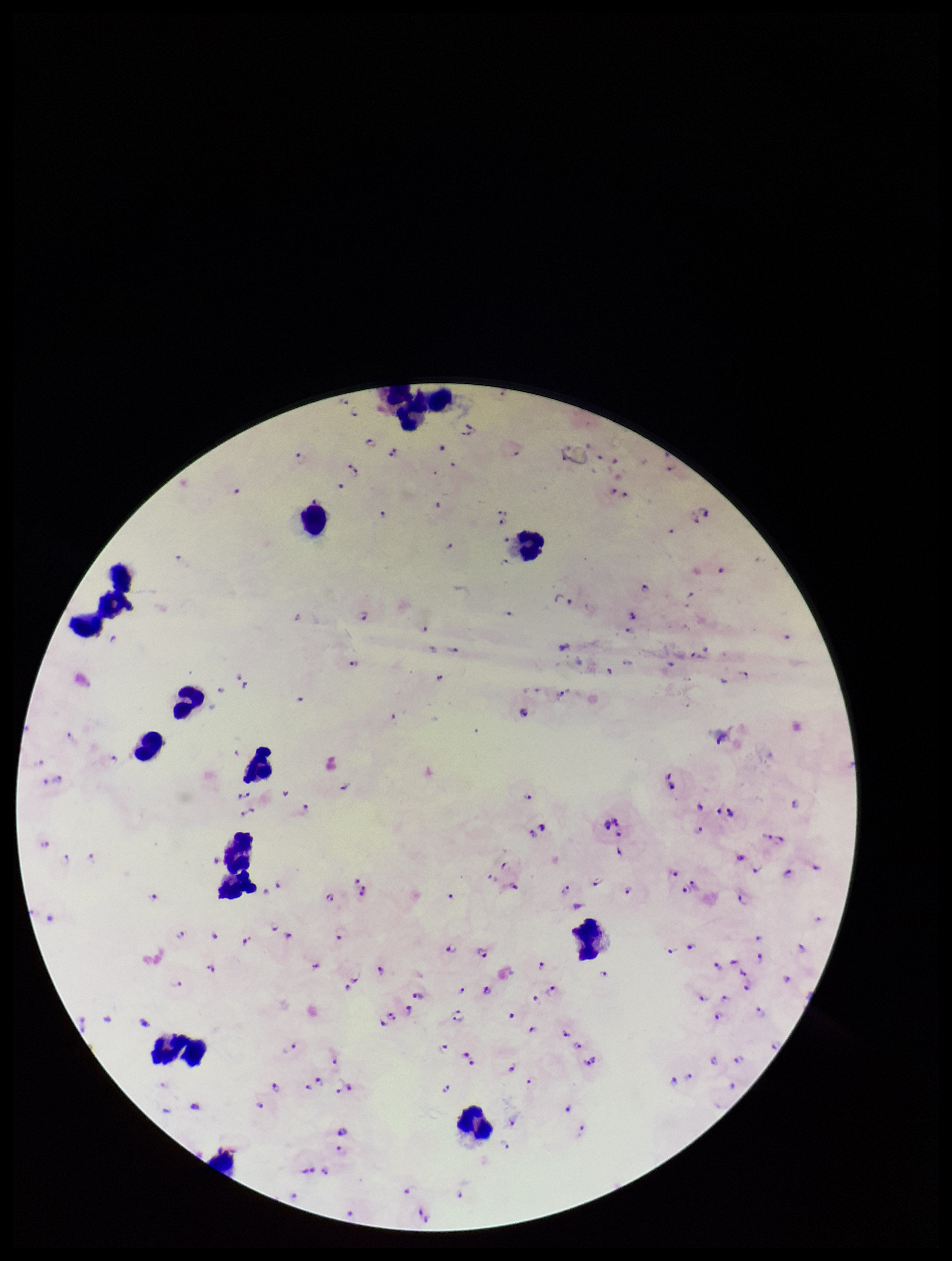

image_size: 952×1261 pixels
species_reported_for_this_patient: Plasmodium falciparum
leukocyte_count: 15
preparation: thick smear
field_of_view: one from this slide
capture: smartphone photograph through the microscope eyepiece
parasite_count: 116
patient_malaria_status: positive
stain: Giemsa
plasmodium_parasites: seen